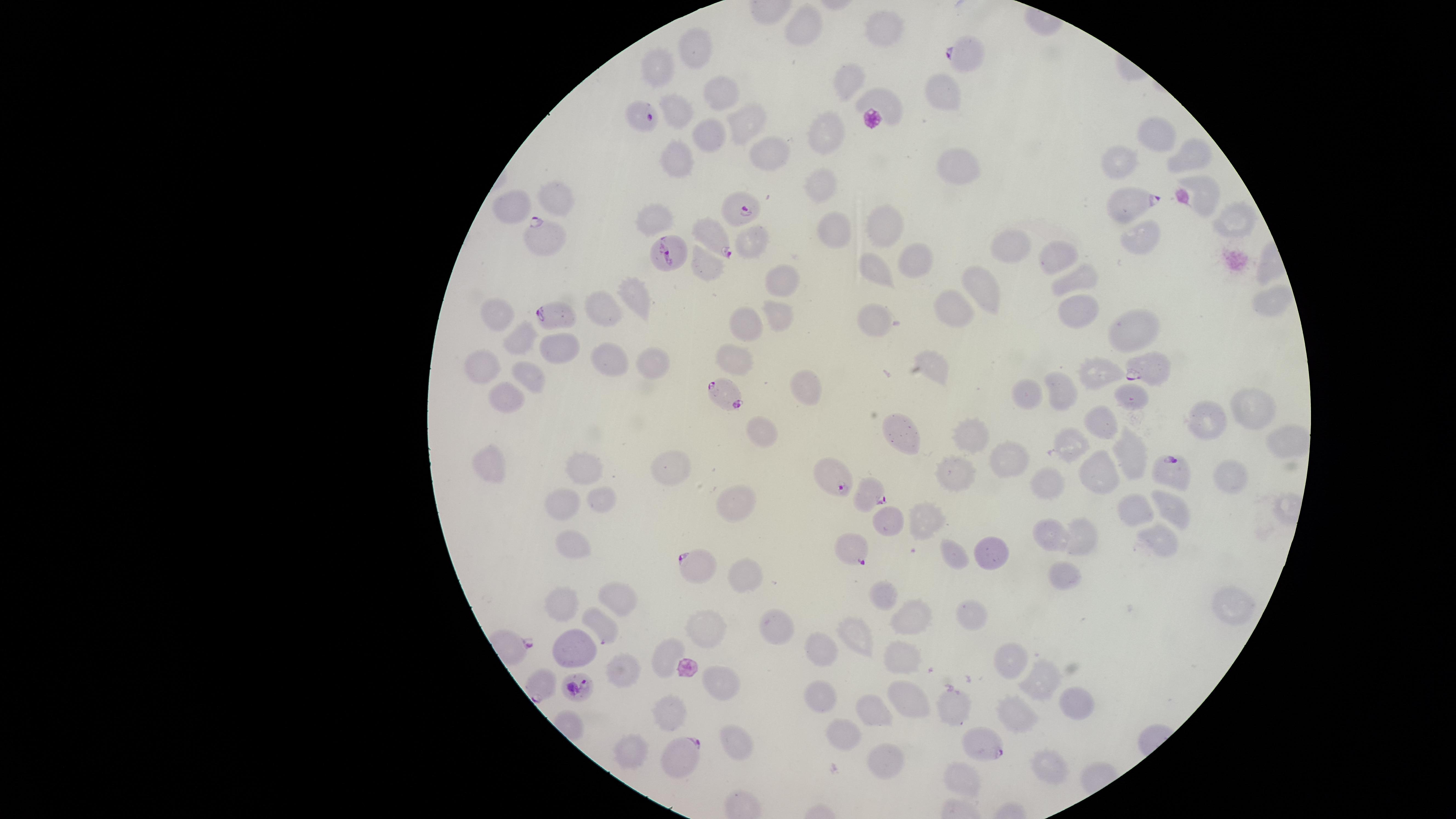
Approximate marker points as {x, y} in pixels.
Summary:
  - Parasitized RBCs: {965, 57}, {644, 117}, {1131, 200}, {741, 210}, {544, 237}, {717, 240}, {671, 251}, {556, 316}, {1149, 368}, {726, 393}, {1169, 467}, {836, 476}, {868, 493}, {850, 547}, {703, 565}, {543, 685}, {581, 687}, {983, 742}, {687, 758}
  - Uninfected RBCs: {801, 29}, {877, 34}, {696, 46}, {656, 67}, {848, 82}, {722, 91}, {942, 93}, {680, 111}, {745, 119}, {827, 133}, {1160, 135}, {701, 138}, {768, 146}, {675, 149}, {1192, 156}, {1125, 158}, {957, 159}, {825, 175}, {558, 197}, {1204, 198}, {512, 204}, {1239, 216}, {650, 222}, {884, 226}, {839, 230}, {1153, 234}, {755, 239}, {1020, 242}, {1063, 255}, {709, 263}, {915, 266}, {872, 270}, {1083, 273}, {781, 279}, {983, 287}, {631, 297}, {1266, 298}, {608, 306}, {1076, 306}, {950, 309}, {500, 310}, {783, 315}, {737, 317}, {882, 328}, {1129, 329}, {516, 336}, {562, 341}, {731, 348}, {654, 356}, {612, 360}, {487, 362}, {935, 365}, {1100, 371}, {537, 372}, {798, 382}, {1063, 389}, {1028, 390}, {506, 397}, {1130, 397}, {1249, 415}, {1105, 418}, {1203, 418}, {899, 426}, {759, 429}, {962, 434}, {1071, 440}, {1128, 449}, {1003, 454}, {493, 461}, {1098, 466}, {657, 468}, {578, 469}, {953, 471}, {1228, 478}, {1047, 481}, {606, 497}, {730, 499}, {555, 503}, {1171, 504}, {1129, 505}, {924, 522}, {891, 523}, {1156, 539}, {1086, 540}, {1059, 541}, {570, 550}, {992, 551}, {956, 555}, {1060, 575}, {749, 578}, {620, 591}, {883, 600}, {563, 604}, {1237, 608}, {969, 616}, {914, 617}, {599, 629}, {705, 630}, {777, 631}, {861, 639}, {822, 644}, {574, 649}, {902, 656}, {667, 657}, {1010, 666}, {625, 669}, {718, 679}, {1044, 683}, {910, 700}, {819, 701}, {1077, 703}, {952, 705}, {1021, 708}, {873, 709}, {673, 712}, {841, 737}, {734, 738}, {638, 746}, {884, 759}, {1053, 768}, {957, 774}
  - Presence: malaria parasites detected
  - Species: Plasmodium falciparum
  - Image size: 1456×819 pixels
  - Stain: Giemsa
  - Visible region: circular
  - Capture: smartphone photograph through the microscope eyepiece
  - Field of view: single
  - Preparation: thin blood film